Report the malaria status of this cell.
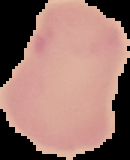
Uninfected.

Summary:
  - Image size: 130×160 pixels
  - Image type: segmented cell region with the area outside set to black
  - Preparation: thin blood film